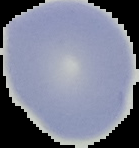

Summary:
  - Malaria status: uninfected
  - Preparation: thin blood smear
  - Image size: 139×148 pixels
  - Image type: segmented cell region with the area outside set to black